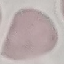

Summary:
  - Result: negative for malaria parasites
  - Image type: automatically extracted cell patch, resized to 64 × 64 pixels
  - Capture: smartphone through the microscope eyepiece
  - Stain: Giemsa
  - Preparation: thin blood film